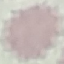

malaria status = uninfected
preparation = thin blood smear
capture = smartphone camera at the microscope eyepiece
image type = cell patch, automatically extracted from a larger field of view and resized to 64 × 64 pixels
stain = Giemsa